Report the malaria status of this cell.
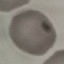
Uninfected.

capture = smartphone camera at the microscope eyepiece
preparation = thin blood smear
image type = cell patch, automatically extracted from a larger field of view and resized to 64 × 64 pixels
stain = Giemsa